Classify this cell by malaria status.
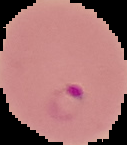

Parasitized.

{
  "image_type": "cell region segmented out of the field of view; surrounding area masked to black",
  "image_size": "127×145 pixels",
  "preparation": "thin blood film"
}